Name the cell type shown.
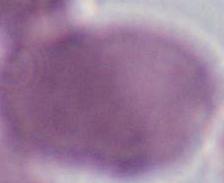

This is an erythrocyte.

1000x magnification. Photomicrograph.